Classify the preparation.
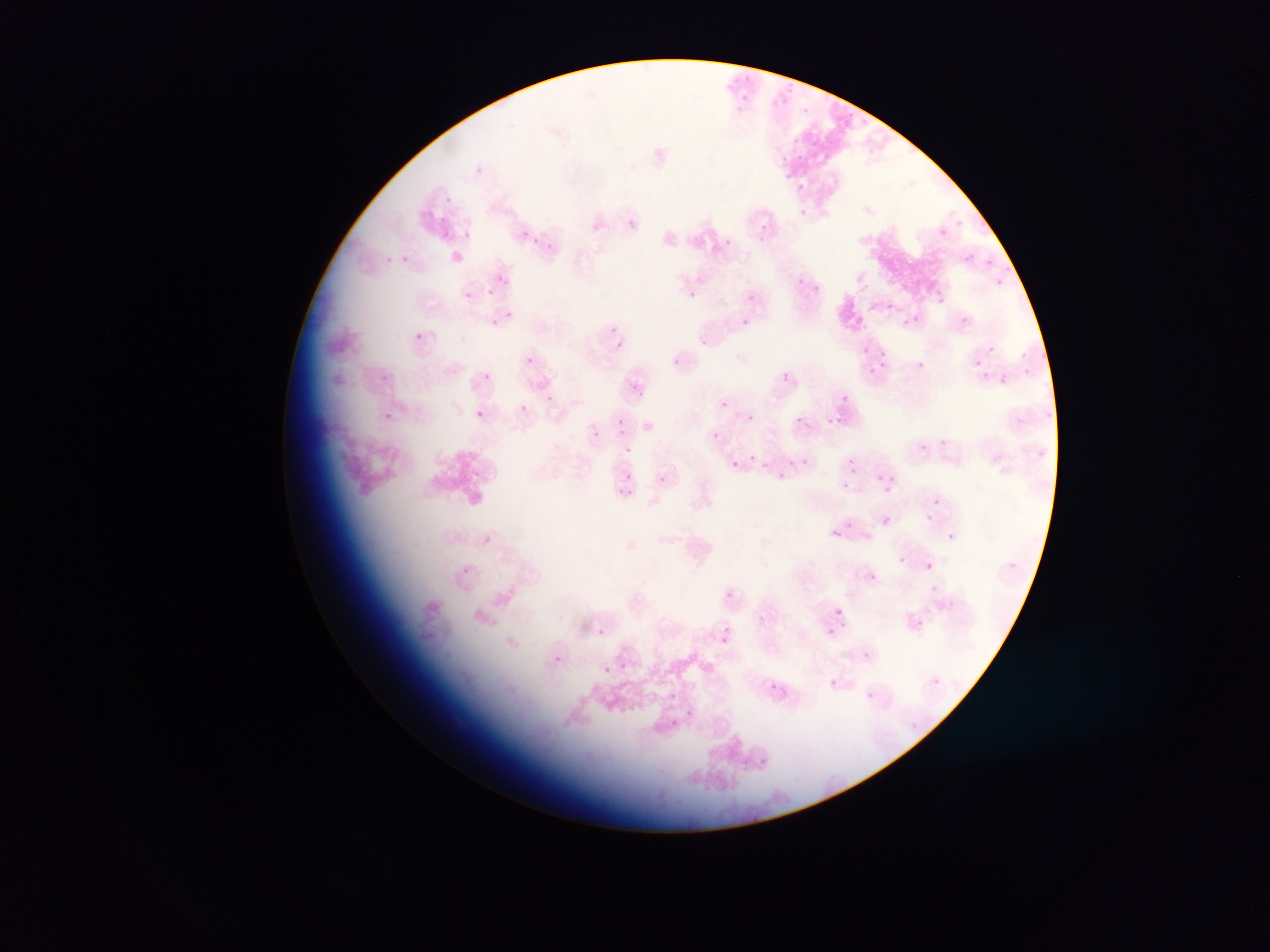
This is a thin smear.

Approximate bounding boxes as left top right bottom in pixels. Plasmodium parasite locations: 722 73 746 85; 788 81 802 92; 739 95 756 116; 774 95 791 111; 800 103 811 115; 791 136 801 141; 814 136 824 151; 795 152 806 162; 780 154 788 163; 478 163 493 173; 786 168 793 179; 795 184 809 197; 441 194 455 210; 799 207 814 220; 628 217 638 233; 955 218 972 230; 751 219 766 230; 983 222 993 236; 938 225 950 240; 439 227 455 240; 463 229 477 244; 521 229 531 240; 759 234 767 244; 530 236 543 246; 723 238 732 247; 540 239 555 254; 963 253 974 268; 402 254 411 261; 380 255 396 266; 983 257 991 267; 1001 262 1010 272; 497 273 508 284; 991 277 1002 291; 798 278 805 287; 486 282 500 298; 815 283 826 298; 464 285 477 299; 689 290 697 299; 746 293 755 302; 939 298 949 314; 889 299 897 315; 500 308 519 320; 911 315 921 326; 485 317 499 329; 961 317 970 325; 740 319 758 334; 601 323 615 339; 413 331 436 348; 699 335 714 354; 609 336 626 355; 987 346 995 354; 879 350 890 362; 1033 350 1053 369; 1017 352 1028 363; 675 354 682 369; 525 356 535 364; 913 359 927 373; 865 365 881 378; 1022 365 1030 376; 984 368 987 382; 1000 370 1009 384; 483 371 492 380; 381 372 393 386; 781 373 789 381; 629 383 647 406; 835 390 851 407; 544 394 561 411; 720 399 729 408; 519 402 537 418; 1045 407 1053 423; 380 410 394 425; 476 410 485 419; 1017 411 1029 431; 615 412 627 436; 826 412 851 425; 746 414 754 421; 791 414 805 429; 643 421 654 430; 591 428 603 438; 712 431 720 440; 935 435 945 450; 920 443 926 453; 1035 443 1049 460; 625 446 633 454; 789 453 795 464; 803 455 813 469; 847 459 857 469; 731 460 739 469; 762 462 769 471; 775 468 783 478; 623 470 632 480; 473 471 486 486; 656 474 665 484; 876 474 886 483; 886 476 897 484; 842 480 850 489; 880 486 892 493; 618 487 633 498; 932 497 940 506; 882 515 890 524; 925 515 933 522; 845 521 854 530; 828 527 842 543; 942 528 954 544; 897 556 905 564; 1006 559 1019 575; 926 562 934 570; 873 574 884 589; 933 581 952 596; 726 589 734 600; 835 608 843 617; 756 616 767 626; 916 617 924 627; 840 620 849 634; 596 627 605 635; 826 627 835 634; 720 632 730 644; 863 649 875 664; 552 653 569 666; 618 661 627 669; 603 666 610 674; 933 674 951 691; 772 679 789 695; 829 679 837 686; 669 688 679 698; 862 691 879 706; 681 711 696 720; 908 718 920 729; 671 721 682 736; 759 751 770 770 | approximate x y pixel centers of objects too small to bound: 865 346; 977 363; 752 456. Collected in Ghana. Mobile-phone photograph taken through the microscope. Single field of view. Image is 1270×952 pixels.